Assess this cell for malaria.
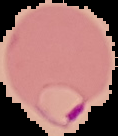
Parasitized.

Summary:
  - Preparation: thin blood film
  - Image type: cell region segmented out of the field of view; surrounding area masked to black
  - Image size: 118×136 pixels